Outline each Babesia divergens-infected red blood cell.
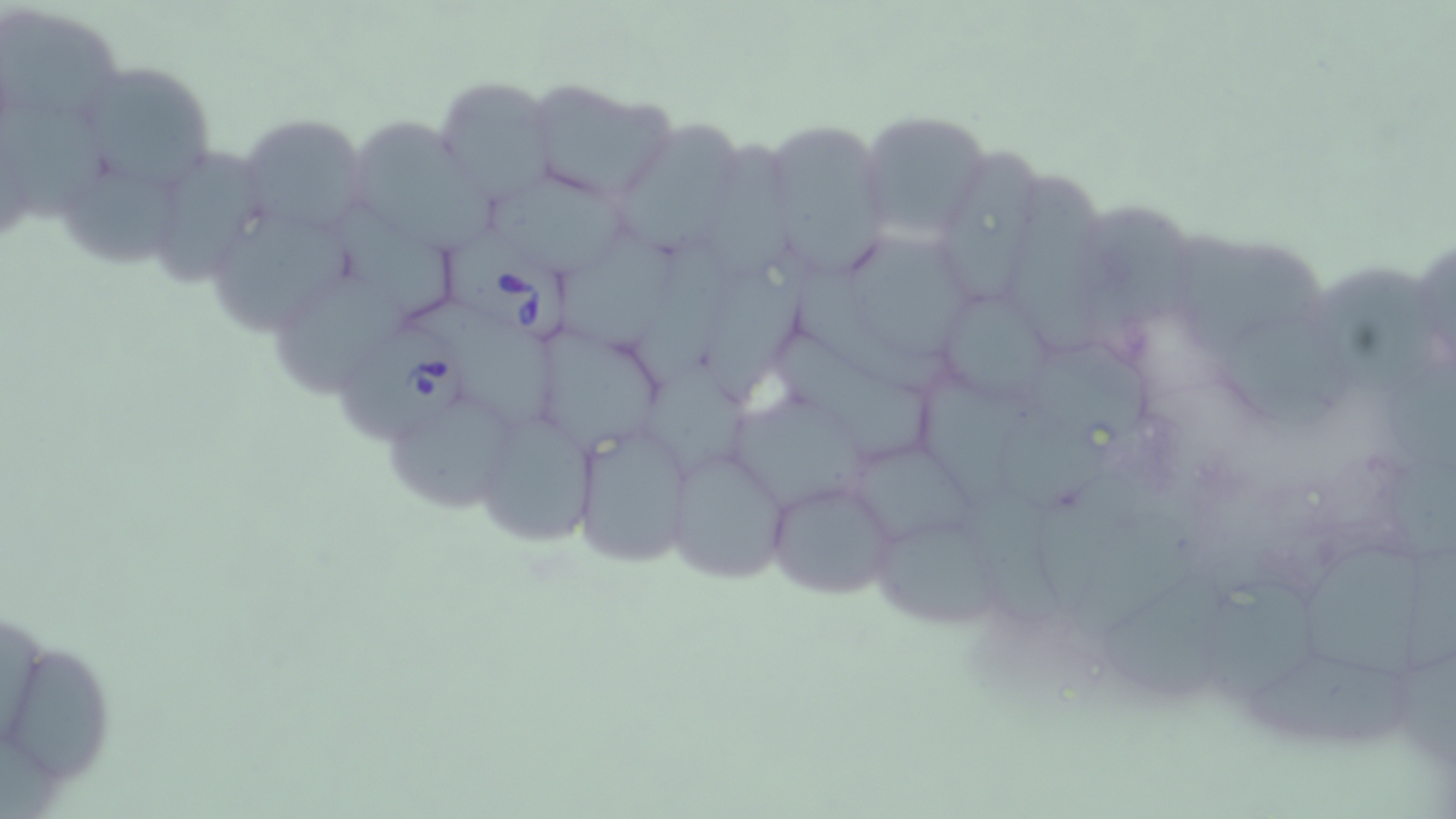

Approximate bounding boxes as [x1, y1, x2, y2] in pixels.
Babesia divergens-infected red blood cells: [438, 224, 574, 346], [339, 328, 469, 444].

Uninfected red blood cell locations: [1, 3, 125, 130], [67, 55, 219, 195], [430, 75, 558, 206], [520, 78, 674, 201], [0, 106, 118, 222], [858, 109, 988, 246], [237, 110, 372, 236], [757, 117, 897, 284], [353, 124, 500, 255], [618, 125, 742, 257], [707, 137, 802, 285], [158, 145, 263, 292], [931, 154, 1050, 308], [1011, 170, 1108, 360], [61, 172, 178, 273], [493, 174, 628, 283], [210, 201, 362, 339], [338, 202, 456, 325], [1085, 210, 1194, 335], [847, 227, 972, 359], [560, 232, 679, 353], [1178, 238, 1329, 352], [633, 243, 736, 394], [1326, 266, 1434, 389], [702, 272, 812, 410], [797, 274, 958, 402], [272, 277, 410, 401], [943, 300, 1056, 401], [411, 305, 562, 431], [775, 322, 932, 464], [1222, 324, 1352, 424], [535, 328, 665, 453], [1036, 352, 1153, 437], [645, 355, 757, 481], [1385, 367, 1456, 469], [923, 377, 1028, 511], [379, 394, 514, 514], [738, 397, 872, 513], [1002, 408, 1119, 509], [486, 418, 597, 543], [570, 427, 694, 564], [845, 443, 983, 544], [666, 445, 792, 584], [1387, 453, 1456, 554], [762, 476, 900, 602], [956, 488, 1079, 630], [1041, 505, 1184, 634], [877, 526, 1011, 626], [1304, 550, 1430, 678], [1101, 570, 1236, 703], [1201, 578, 1318, 707], [1250, 646, 1415, 744], [12, 647, 108, 794], [1406, 654, 1456, 769]. Slide-level diagnosis: Babesia divergens. Image is 1456×819 pixels. Thin blood smear. Single field of view. Captured at 1000x magnification. Light microscopy. May-Grünwald-Giemsa-stained preparation.